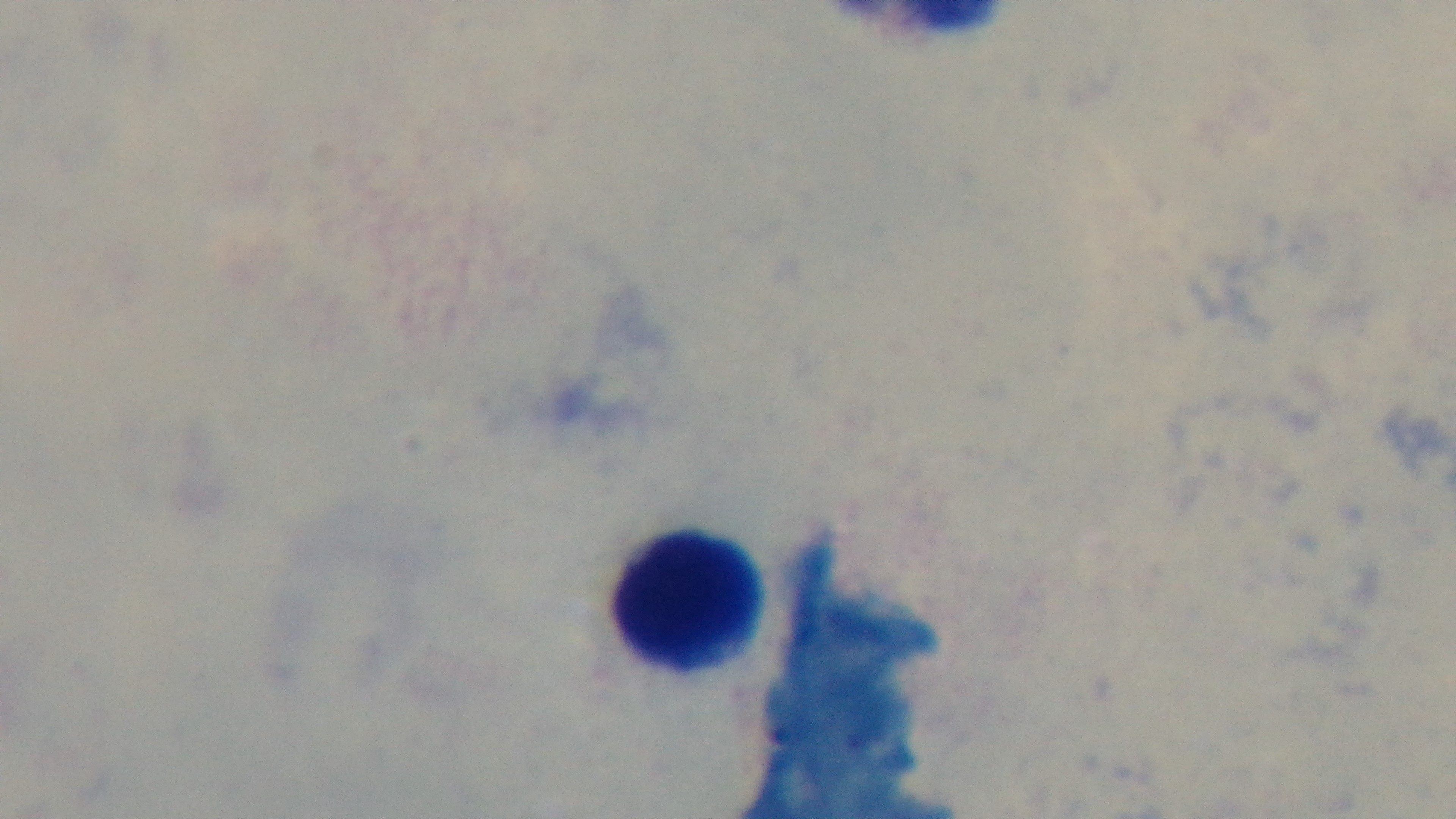
Summary:
  - Field of view: single
  - Preparation: thick blood film
  - Stain: Giemsa
  - Malaria status: uninfected
  - Modality: light microscopy
  - Capture: mounted 4K digital camera
  - Objective: 100x oil immersion